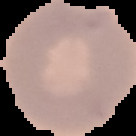

Summary:
  - Result: no Plasmodium parasites seen
  - Image size: 136×136 pixels
  - Preparation: thin blood smear
  - Image type: segmented cell region on a black background